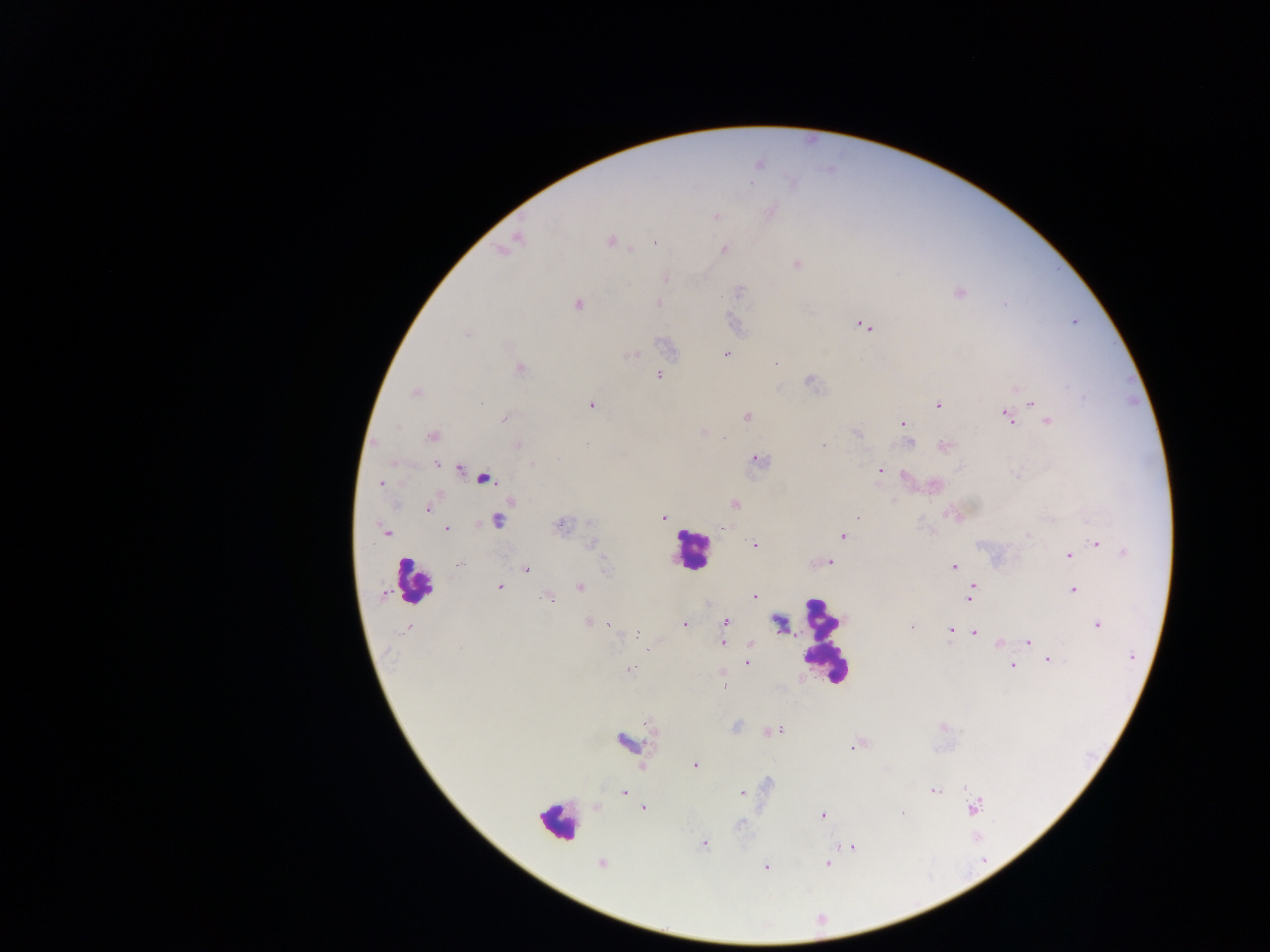 Approximate centers as {x, y} in pixels. Plasmodium parasite locations: {759, 165}, {716, 216}, {517, 238}, {610, 241}, {655, 243}, {724, 249}, {796, 264}, {666, 279}, {740, 291}, {959, 293}, {658, 303}, {578, 304}, {864, 326}, {468, 334}, {726, 354}, {633, 355}, {776, 363}, {519, 369}, {659, 375}, {811, 383}, {415, 393}, {1084, 397}, {1032, 403}, {591, 405}, {937, 405}, {746, 416}, {1006, 416}, {504, 418}, {1048, 422}, {903, 424}, {858, 434}, {433, 435}, {724, 438}, {908, 442}, {517, 445}, {824, 445}, {946, 446}, {759, 460}, {437, 464}, {533, 464}, {879, 470}, {460, 471}, {381, 483}, {510, 501}, {734, 504}, {427, 509}, {663, 517}, {857, 517}, {496, 521}, {560, 526}, {447, 529}, {723, 529}, {385, 531}, {844, 536}, {1028, 536}, {1097, 543}, {591, 544}, {755, 544}, {1124, 553}, {1068, 555}, {829, 562}, {461, 563}, {954, 567}, {526, 569}, {499, 587}, {580, 587}, {972, 587}, {1073, 590}, {755, 596}, {546, 597}, {969, 597}, {726, 621}, {589, 622}, {685, 624}, {1097, 624}, {912, 626}, {407, 628}, {950, 631}, {974, 632}, {637, 634}, {1028, 642}, {723, 643}, {999, 644}, {749, 645}, {1049, 660}, {747, 663}, {1013, 666}, {631, 669}, {724, 688}, {775, 730}, {626, 741}, {854, 747}, {695, 765}, {768, 783}, {934, 791}, {624, 793}, {742, 794}, {644, 807}, {974, 807}, {902, 814}, {823, 815}, {740, 823}, {704, 843}, {852, 847}, {602, 864}, {826, 865}, {765, 866}. Leukocyte locations: {485, 478}, {690, 550}, {413, 582}, {825, 640}, {557, 823}. Thick blood smear. Mobile-phone photograph taken through the microscope. Sample from Ghana. Image is 1270×952 pixels. Single field of view.